Report the malaria status of this cell.
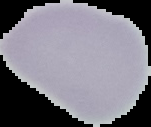
It is uninfected.

From a thin blood film. Cell region segmented out of the field of view; the surrounding area is masked to black. Image is 151×127 pixels.